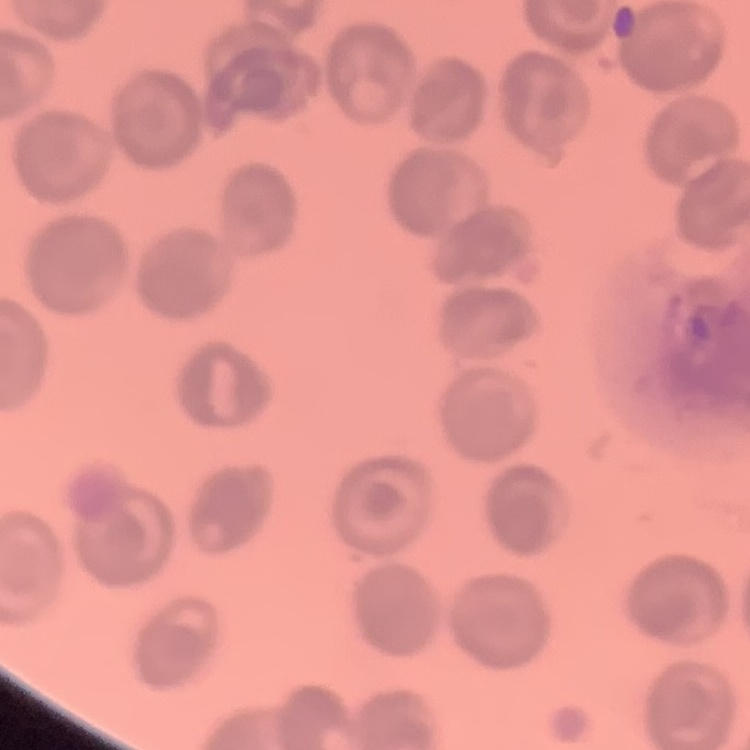

erythrocyte morphology = no rouleaux formation
preparation = thin blood smear
stain = Field's or Giemsa
image type = one tile cut from a larger photomicrograph